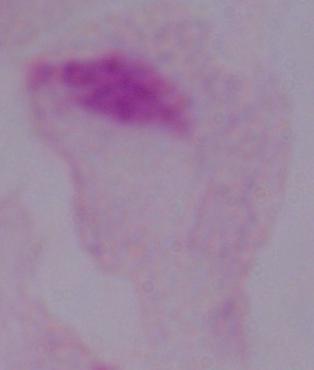

Summary:
  - Magnification: 1000x
  - Modality: photomicrograph
  - Identification: trichomonad